Comment on the morphology of the erythrocytes.
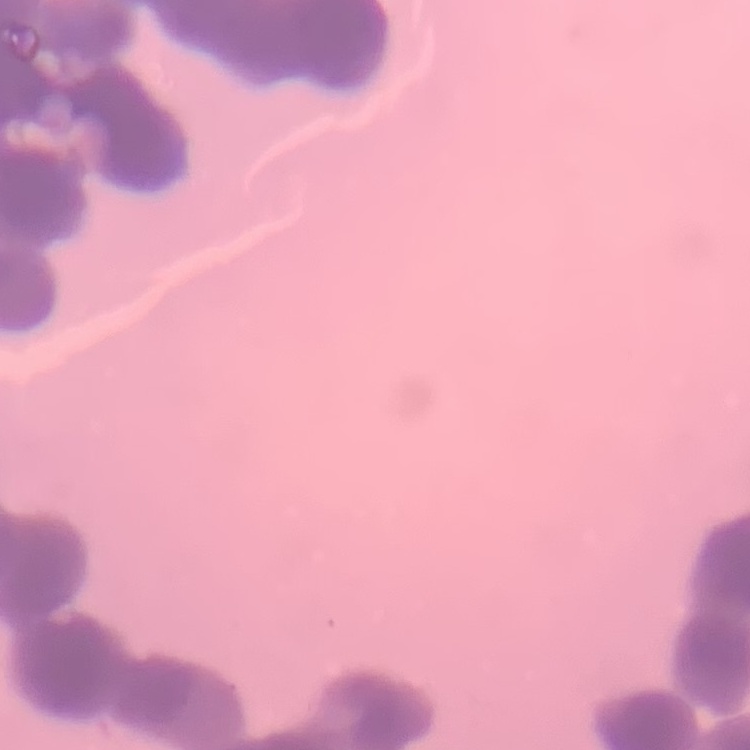
They show rouleaux formation.

Thin peripheral smear. Square crop of a larger photomicrograph. Stained with either Field's or Giemsa.